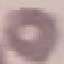 Result: no malaria parasites detected. Thin blood film. Acquired by smartphone through the microscope eyepiece. Automatically extracted cell patch, resized to 64 × 64 pixels. Giemsa stain.